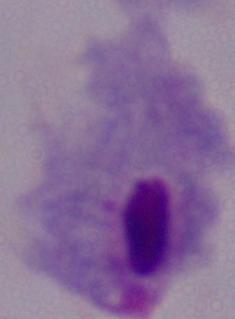
Summary:
  - Identification: trichomonad
  - Modality: micrograph
  - Magnification: 1000x